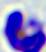

400x magnification. Photomicrograph. A leukocyte is shown.